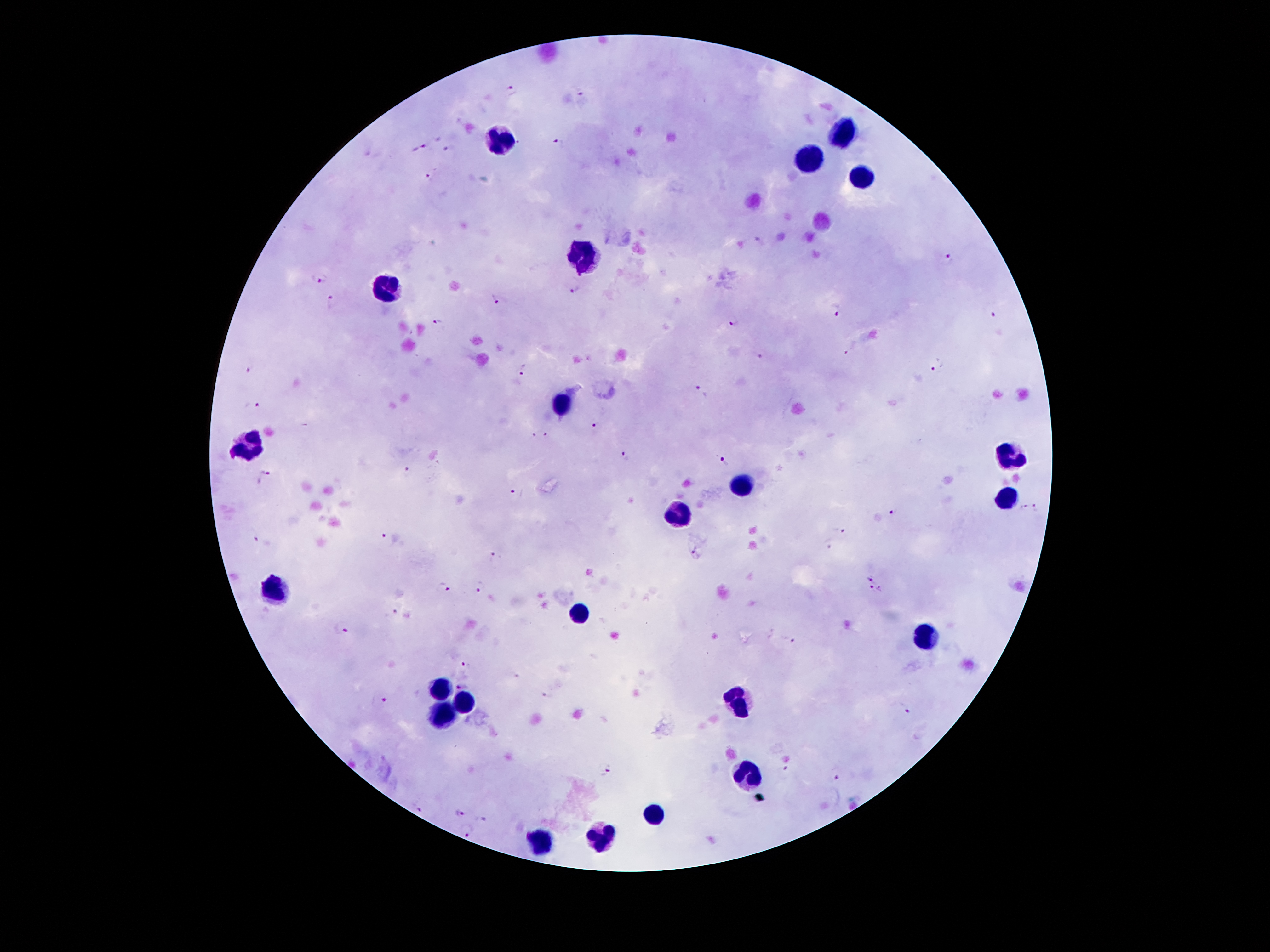

coordinate format = approximate centers as [x, y] in pixels
leukocyte locations = [839, 133], [500, 141], [810, 159], [865, 177], [585, 253], [386, 290], [564, 402], [244, 443], [1014, 454], [740, 483], [1007, 498], [678, 509], [279, 590], [579, 612], [926, 634], [439, 692], [739, 702], [464, 704], [437, 718], [749, 778], [657, 813], [604, 840], [541, 842]
malaria parasite locations = [513, 90], [583, 94], [559, 141], [419, 147], [447, 150], [430, 177], [760, 241], [948, 259], [318, 281], [574, 289], [497, 297], [331, 299], [835, 312], [994, 317], [732, 322], [440, 323], [759, 355], [249, 366], [525, 368], [937, 368], [702, 393], [251, 406], [594, 428], [549, 436], [532, 437], [626, 455], [724, 461], [406, 472], [265, 476], [517, 493], [1038, 507], [1023, 508], [892, 513], [843, 529], [252, 536], [385, 538], [829, 544], [698, 552], [495, 556], [873, 578], [479, 586], [444, 588], [869, 590], [880, 590], [391, 614], [342, 628], [790, 641], [467, 665], [516, 675], [461, 684], [549, 695], [381, 700], [902, 709], [784, 769], [606, 772], [835, 780], [418, 808], [460, 811], [480, 819], [467, 826]
preparation = thick peripheral-blood smear
image size = 1270×952 pixels
capture = smartphone camera through the microscope eyepiece
patient malaria status = infected with Plasmodium falciparum
field of view = one from this slide
stain = Giemsa
magnification = 100x